Report the malaria status of this cell.
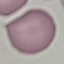
Uninfected.

Summary:
  - Image type: cell patch, automatically extracted from a larger field of view and resized to 64 × 64 pixels
  - Capture: smartphone through the microscope eyepiece
  - Preparation: thin blood smear
  - Stain: Giemsa